Outline each blood parasite and name the species.
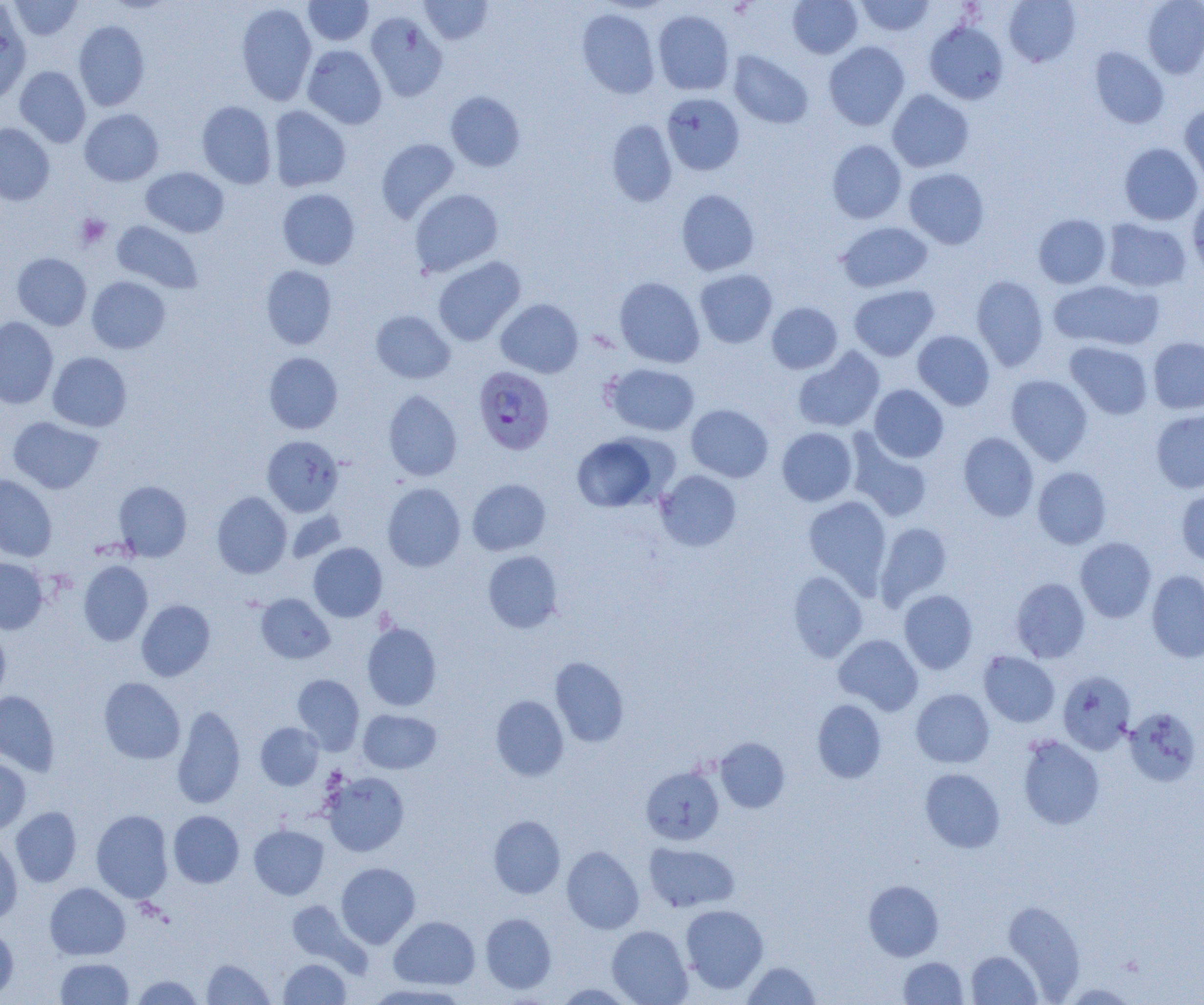
Approximate bounding boxes as (x1,y1)-(x2,y2) corner pairs in pixels.
Plasmodium falciparum-infected red blood cells: (473,366)-(555,454).
No Plasmodium ovale, Plasmodium malariae, Plasmodium vivax, Babesia divergens, or Trypanosoma brucei observed.

Summary:
  - Uninfected red blood cell locations: (8,0)-(83,41), (303,0)-(373,46), (419,0)-(493,45), (788,0)-(862,59), (856,0)-(935,36), (1004,0)-(1081,67), (1142,0)-(1204,78), (235,3)-(317,105), (0,4)-(31,104), (576,8)-(660,98), (653,9)-(734,95), (365,12)-(447,101), (74,20)-(150,112), (924,20)-(1009,105), (823,41)-(910,130), (302,45)-(387,129), (1089,47)-(1169,129), (727,50)-(814,128), (15,66)-(91,147), (887,89)-(974,173), (445,91)-(525,171), (661,93)-(745,175), (197,101)-(276,188), (1180,104)-(1204,190), (268,106)-(351,191), (79,108)-(164,186), (606,119)-(677,206), (0,123)-(54,205), (377,138)-(460,223), (827,140)-(907,224), (1119,143)-(1203,225), (141,167)-(229,237), (904,168)-(989,249), (277,188)-(360,270), (409,189)-(503,276), (676,189)-(760,275), (1187,192)-(1204,278), (1033,214)-(1111,288), (1103,218)-(1191,292), (111,220)-(203,293), (837,222)-(932,292), (12,253)-(91,330), (432,256)-(526,346), (260,265)-(337,349), (694,269)-(777,347), (970,275)-(1049,371), (86,276)-(171,354), (614,277)-(705,368), (1048,279)-(1164,351), (848,284)-(939,361), (495,298)-(583,378), (767,302)-(842,373), (371,310)-(455,383), (0,316)-(58,409), (913,330)-(995,410), (1148,337)-(1204,414), (1065,341)-(1153,419), (792,346)-(885,433), (48,352)-(132,432), (264,352)-(343,434), (604,363)-(700,436), (1006,375)-(1093,465), (869,384)-(949,462), (383,390)-(462,481), (686,404)-(773,482), (1151,409)-(1204,493), (8,416)-(105,494), (777,427)-(857,506), (958,432)-(1039,521), (570,433)-(670,512), (846,434)-(933,522), (262,435)-(343,516), (1032,467)-(1111,549), (655,470)-(742,551), (0,474)-(57,561), (467,478)-(551,555), (113,481)-(192,561), (382,483)-(465,571), (1176,485)-(1204,566), (212,492)-(292,578), (803,495)-(892,592), (286,509)-(347,564), (875,521)-(953,608), (1074,537)-(1156,623), (308,542)-(387,622), (483,550)-(564,633), (0,557)-(48,634), (78,560)-(153,646), (1146,570)-(1204,663), (788,571)-(867,662), (1010,578)-(1090,662), (898,590)-(978,674), (256,593)-(335,664), (136,599)-(215,681), (361,621)-(442,711), (0,626)-(10,704), (833,634)-(923,715), (979,651)-(1060,727), (550,657)-(629,747), (1058,671)-(1136,754), (292,674)-(365,754), (99,677)-(185,764), (911,689)-(994,768), (0,691)-(60,775), (490,695)-(569,781), (812,699)-(886,783), (171,704)-(246,809), (1124,708)-(1201,787), (359,709)-(441,774), (255,722)-(324,789), (1017,735)-(1105,830), (715,738)-(790,813), (0,757)-(31,834), (641,765)-(724,845), (920,768)-(1005,853), (321,771)-(409,856), (11,807)-(81,886), (91,809)-(173,903), (168,810)-(244,887), (488,815)-(565,898), (249,825)-(328,899), (0,835)-(22,924), (644,842)-(740,913), (562,846)-(643,933), (336,862)-(420,947), (863,880)-(944,961), (45,882)-(130,960), (285,899)-(368,973), (1002,901)-(1085,1000), (680,904)-(768,993), (480,913)-(557,994), (389,916)-(480,990), (0,925)-(19,1000), (607,925)-(692,1005), (966,950)-(1041,1004), (898,956)-(968,1004), (55,957)-(134,1004), (202,958)-(274,1004), (278,958)-(351,1004), (741,961)-(820,1004), (130,975)-(204,1004), (364,982)-(472,1004), (554,983)-(636,1004)
  - Platelet locations: (76,214)-(111,249)
  - Slide-level diagnosis: Plasmodium falciparum
  - Image size: 1204×1005 pixels
  - Preparation: thin blood film
  - Field of view: single
  - Magnification: 1000x
  - Modality: optical microscopy